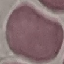
Summary:
  - Result: no malaria parasites detected
  - Capture: smartphone through the microscope eyepiece
  - Image type: automatically extracted cell patch, resized to 64 × 64 pixels
  - Preparation: thin blood film
  - Stain: Giemsa